Describe the morphology of the erythrocytes.
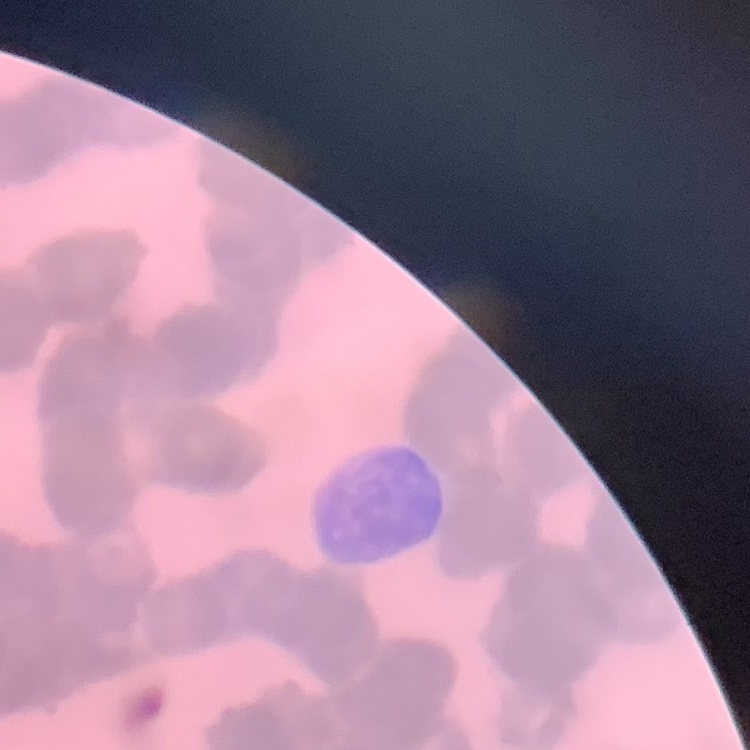
They show rouleaux formation.

Square crop of a larger photomicrograph. Stained with either Field's or Giemsa. Thin blood film.